Assess the morphology of the red blood cells.
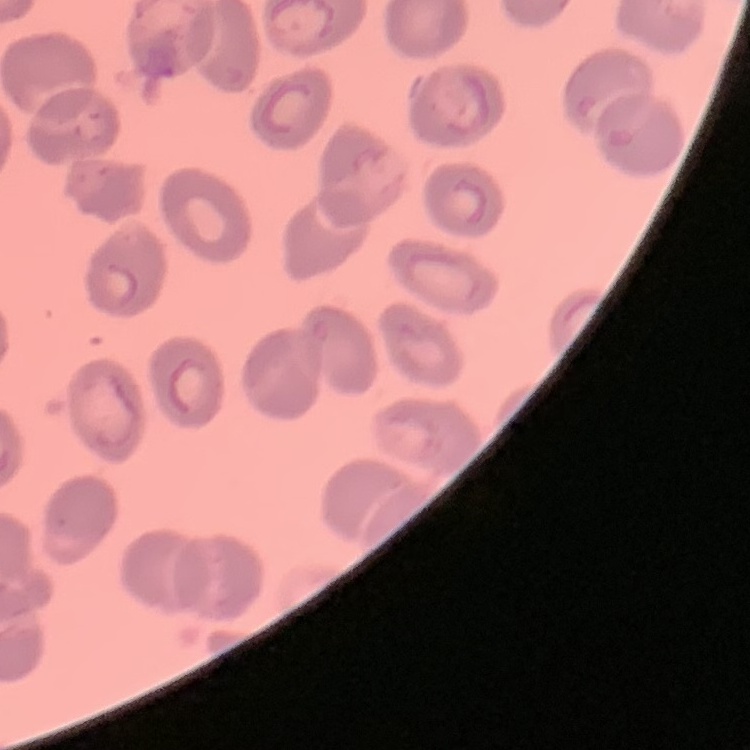

They show no rouleaux formation.

One tile cut from a larger photomicrograph. Field's or Giemsa stain. Thin peripheral smear.